Describe the morphology of the erythrocytes.
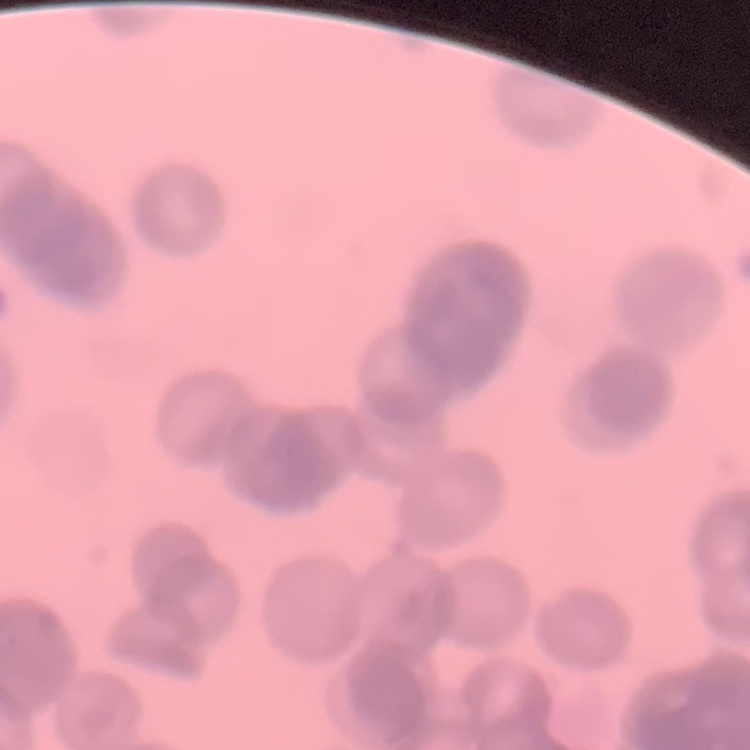

They show rouleaux formation.

Summary:
  - Stain: Field's or Giemsa
  - Preparation: thin blood smear
  - Image type: square crop of a larger photomicrograph